Assess the morphology of the red blood cells.
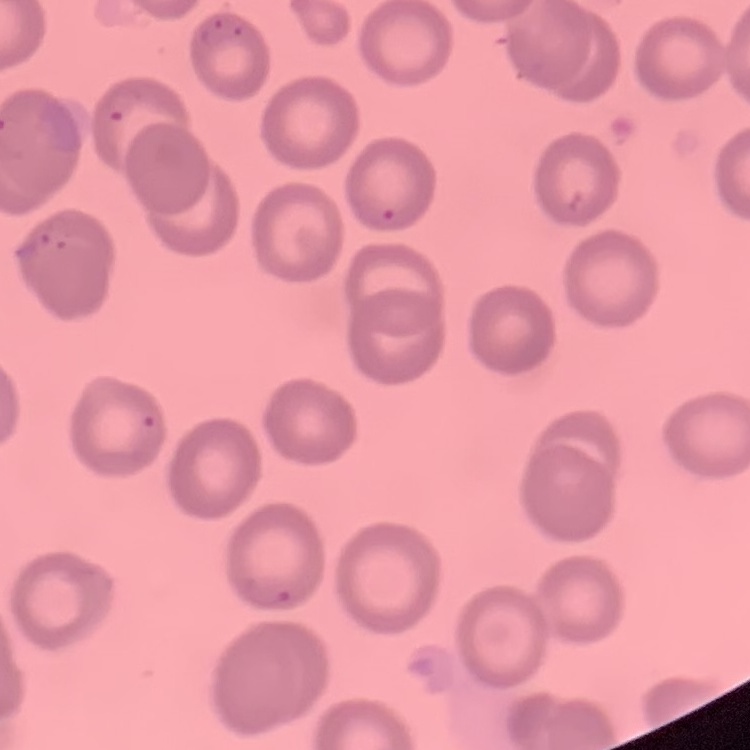
No rouleaux formation.

preparation = thin blood film
stain = Field's or Giemsa
image type = square crop of a larger photomicrograph